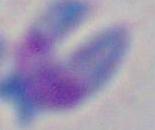
Micrograph. Toxoplasma gondii is shown. 1000x magnification.